Assess this cell for malaria.
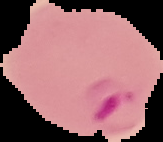
It is parasitized.

Summary:
  - Image type: cell region segmented out of the field of view; surrounding area masked to black
  - Image size: 163×142 pixels
  - Preparation: thin blood film